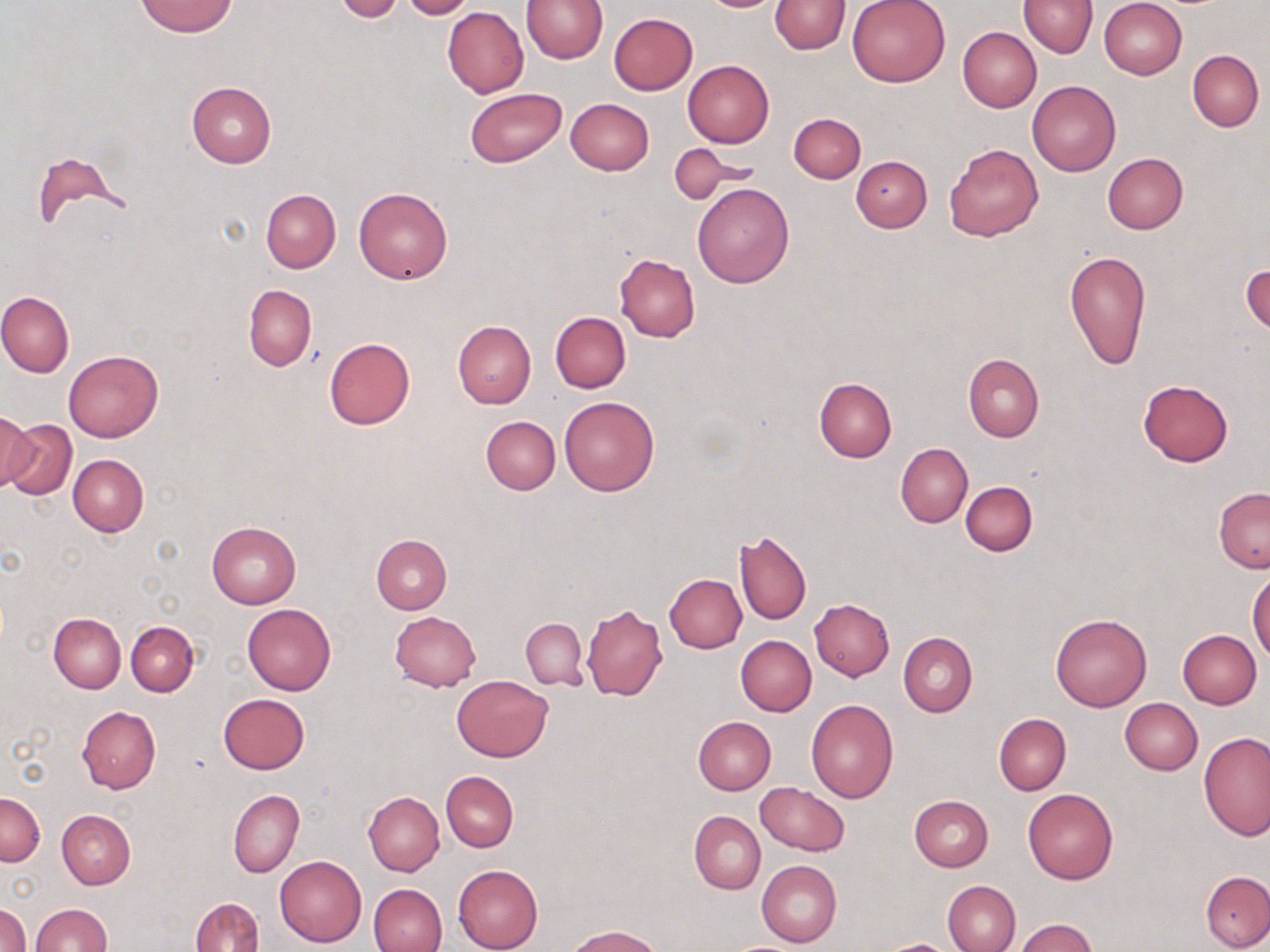 Approximate bounding boxes as [x1, y1, x2, y2] in pixels. Uninfected red blood cell locations: [399, 0, 475, 20], [520, 0, 607, 63], [697, 0, 785, 12], [847, 0, 950, 87], [1019, 0, 1096, 58], [1100, 0, 1188, 79], [136, 1, 237, 37], [334, 1, 404, 22], [767, 1, 938, 64], [769, 1, 849, 54], [442, 8, 528, 97], [607, 13, 698, 95], [957, 27, 1041, 112], [1187, 50, 1264, 130], [682, 61, 774, 148], [187, 81, 276, 168], [1027, 81, 1121, 177], [465, 88, 567, 167], [565, 98, 654, 175], [789, 113, 865, 183], [944, 144, 1043, 242], [670, 146, 746, 203], [30, 152, 124, 232], [1103, 153, 1187, 234], [851, 156, 932, 233], [692, 182, 794, 287], [353, 187, 453, 284], [261, 190, 340, 273], [1063, 249, 1151, 371], [614, 253, 701, 341], [1242, 260, 1269, 336], [243, 285, 317, 371], [0, 291, 74, 378], [550, 312, 631, 392], [453, 320, 536, 408], [323, 337, 414, 431], [64, 350, 163, 442], [963, 353, 1044, 443], [814, 377, 896, 462], [1138, 379, 1233, 467], [559, 396, 659, 497], [0, 410, 35, 493], [3, 417, 77, 501], [480, 417, 560, 495], [895, 444, 972, 527], [67, 454, 148, 536], [961, 481, 1036, 556], [1214, 487, 1270, 574], [207, 522, 301, 608], [734, 530, 812, 625], [370, 535, 451, 614], [1248, 568, 1269, 661], [665, 574, 746, 652], [810, 599, 895, 680], [243, 602, 335, 694], [581, 604, 666, 702], [389, 611, 480, 692], [1050, 613, 1152, 711], [49, 614, 125, 693], [521, 618, 588, 690], [126, 621, 198, 695], [1177, 630, 1260, 709], [898, 632, 977, 717], [735, 636, 815, 716], [452, 676, 552, 762], [218, 693, 310, 775], [1120, 697, 1202, 774], [806, 699, 899, 803], [76, 706, 159, 793], [994, 714, 1071, 794], [693, 717, 775, 795], [1198, 732, 1269, 842], [442, 772, 518, 852], [756, 783, 848, 855], [1022, 788, 1118, 885], [228, 789, 303, 878], [363, 791, 444, 876], [0, 793, 45, 866], [909, 795, 993, 872], [56, 810, 135, 888], [689, 811, 765, 894], [275, 855, 367, 946], [756, 860, 841, 948], [453, 864, 542, 952], [1200, 870, 1270, 950], [942, 880, 1020, 952], [368, 883, 447, 951], [190, 897, 263, 952], [0, 902, 30, 952], [29, 903, 112, 951], [1012, 919, 1099, 952], [566, 925, 662, 952], [876, 939, 959, 951]. Slide-level diagnosis: negative for blood parasites. Thin blood smear. Image is 1270×952 pixels. Single field of view. Optical microscopy. Captured at 1000x magnification. May-Grünwald-Giemsa stain.